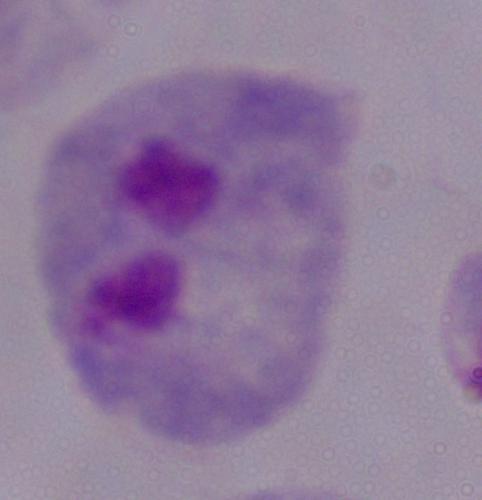 Micrograph. 1000x magnification. A trichomonad is seen.